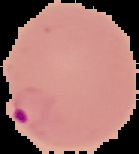

Summary:
  - Image type: segmented cell region on a black background
  - Malaria status: parasitized
  - Preparation: thin blood film
  - Image size: 139×154 pixels